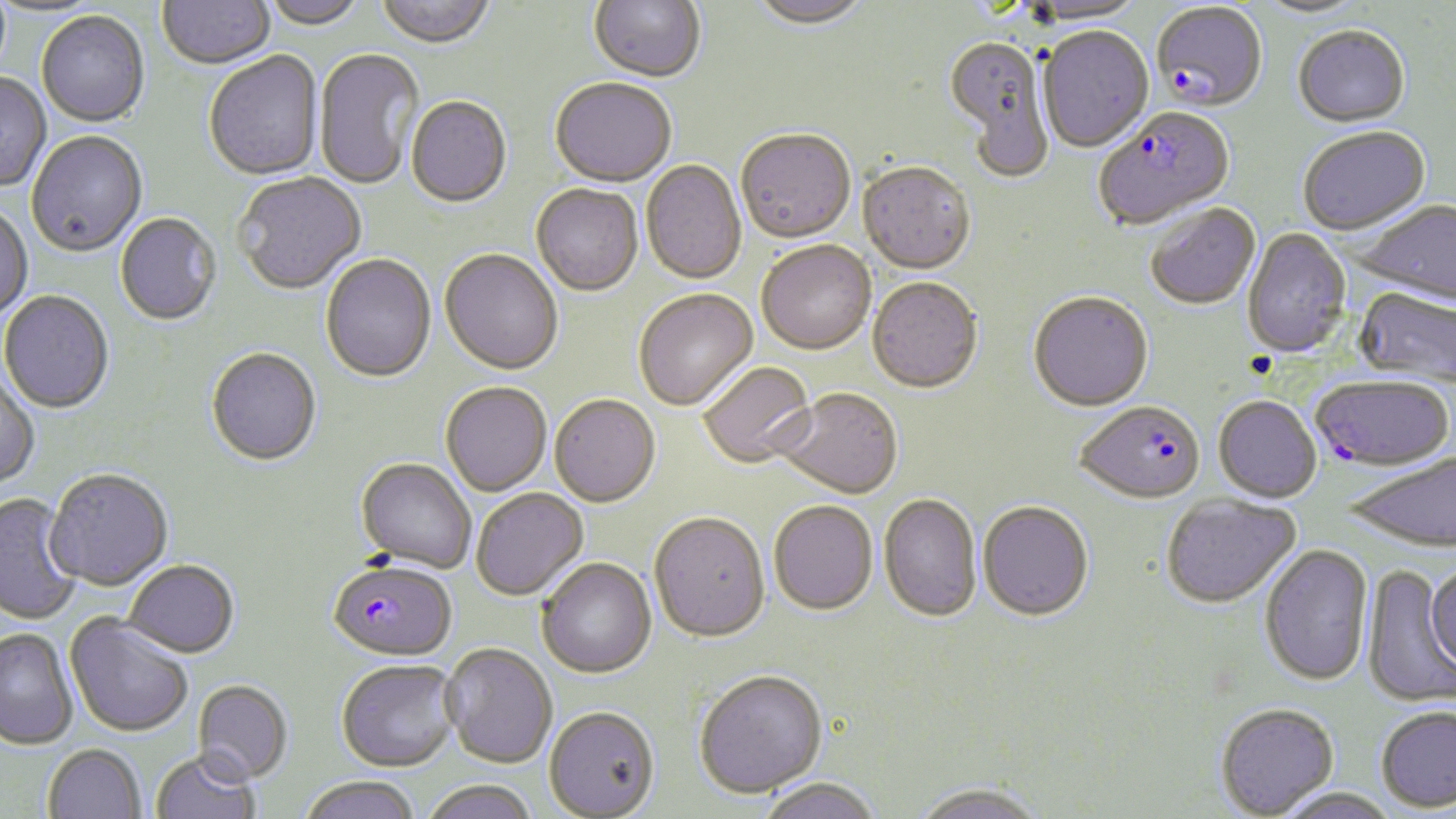

Approximate bounding boxes as (x1,y1)-(x2,y2) corner pairs in pixels. Uninfected red blood cell locations: (157,0)-(275,70), (260,0)-(367,30), (376,0)-(495,50), (589,0)-(705,84), (1252,0)-(1372,20), (748,1)-(872,33), (1022,1)-(1149,27), (36,11)-(150,127), (1292,25)-(1410,128), (1038,28)-(1153,153), (943,38)-(1055,179), (313,48)-(425,191), (204,52)-(323,181), (0,71)-(51,192), (550,80)-(676,189), (406,98)-(512,210), (1297,126)-(1431,236), (26,131)-(147,258), (735,131)-(856,246), (641,161)-(747,285), (857,163)-(975,275), (234,172)-(366,295), (531,185)-(643,297), (1354,198)-(1456,307), (0,204)-(33,322), (1145,204)-(1260,310), (115,213)-(222,326), (1243,228)-(1351,357), (756,243)-(876,356), (439,250)-(563,376), (320,254)-(436,383), (867,278)-(982,395), (1355,287)-(1456,388), (1,290)-(114,414), (634,290)-(758,411), (1028,292)-(1153,412), (206,347)-(321,466), (699,361)-(817,469), (0,372)-(40,490), (441,382)-(552,496), (774,389)-(902,500), (550,395)-(660,507), (1213,396)-(1321,503), (1346,452)-(1456,552), (356,458)-(477,573), (44,468)-(173,591), (471,488)-(588,599), (0,493)-(82,626), (1161,493)-(1300,608), (879,494)-(982,622), (769,501)-(878,616), (977,501)-(1094,621), (649,512)-(770,644), (1260,544)-(1373,686), (537,558)-(657,678), (123,559)-(240,658), (1425,560)-(1456,676), (1361,566)-(1456,708), (65,614)-(195,738), (0,628)-(79,750), (441,642)-(557,768), (336,658)-(460,771), (693,669)-(828,798), (192,679)-(294,784), (1215,702)-(1338,817), (1376,705)-(1456,812), (544,706)-(660,818), (42,744)-(146,819), (150,749)-(261,819), (300,775)-(420,819), (755,777)-(883,819), (419,779)-(539,819), (910,781)-(1049,819), (1270,787)-(1402,819). Plasmodium falciparum-infected red blood cell locations: (1152,3)-(1267,113), (1094,108)-(1235,231), (1310,374)-(1454,471), (1075,401)-(1206,505), (327,559)-(458,661). Slide-level diagnosis: Plasmodium falciparum. May-Grünwald-Giemsa stain. Image is 1456×819 pixels. Optical microscopy. Captured at 1000x magnification. Thin blood smear. One field of a larger specimen.